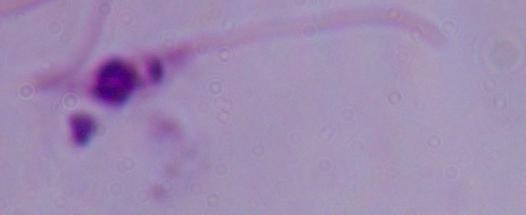
Captured at 1000x magnification. A Leishmania parasite is shown. Micrograph.